Report the malaria status of this cell.
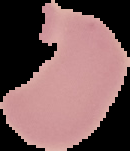

It is uninfected.

Summary:
  - Preparation: thin blood smear
  - Image type: cell region segmented out of the field of view; surrounding area masked to black
  - Image size: 130×151 pixels